Name the parasite shown.
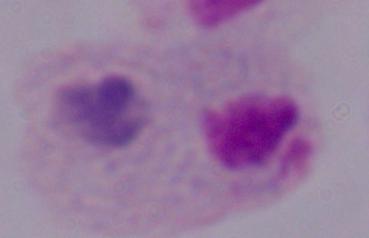

This is a trichomonad.

Photomicrograph. Captured at 1000x magnification.